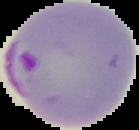

From a thin blood film. Cell region segmented out of the field of view; the surrounding area is masked to black. Image is 139×130 pixels. Result: Plasmodium parasites detected.